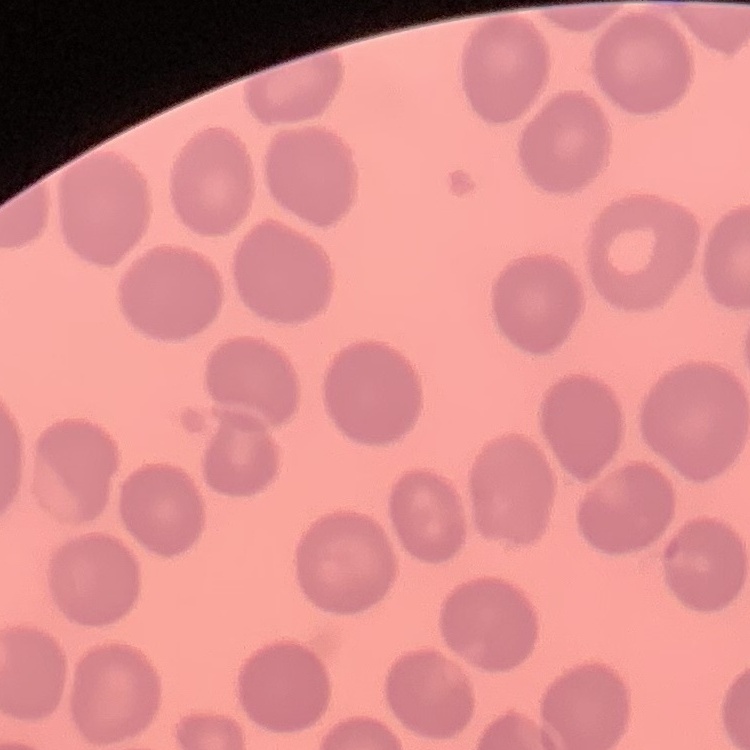
Summary:
  - Erythrocyte morphology: no rouleaux formation
  - Image type: one tile cut from a larger photomicrograph
  - Stain: Field's or Giemsa
  - Preparation: thin blood film